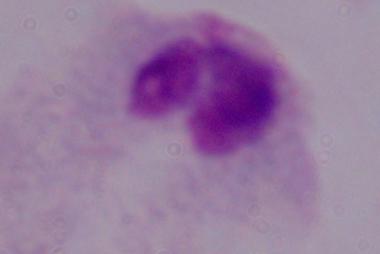

{
  "magnification": "1000x",
  "modality": "micrograph",
  "identification": "trichomonad"
}